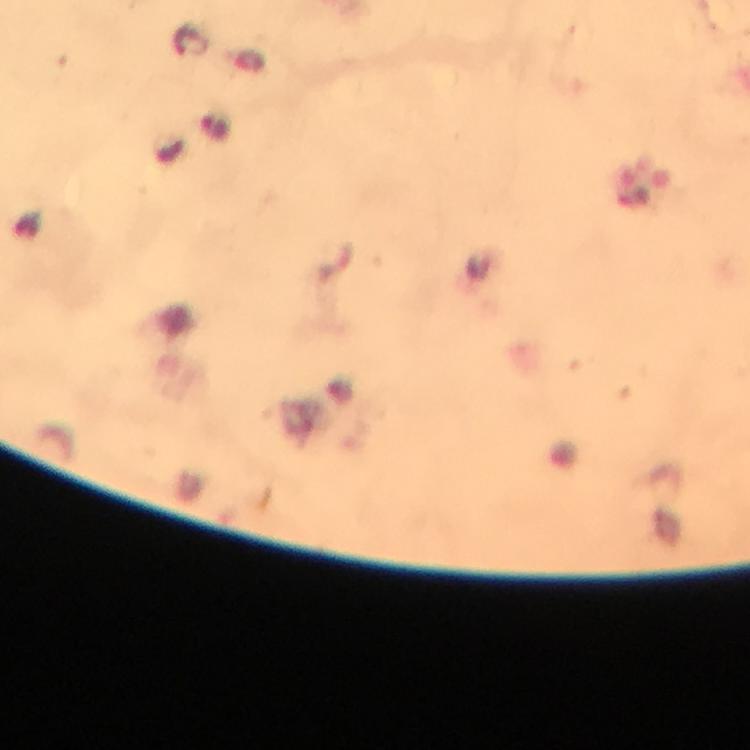
Approximate centers as (x, y) in pixels.
Summary:
  - Malaria parasite locations: (191, 45), (218, 127)
  - Immersion oil: applied
  - Cropped from: a single field of view
  - Preparation: thick blood film
  - Context: from a malaria diagnostic workup
  - Magnification: 100x
  - Image size: 750×750 pixels
  - Capture: smartphone camera through the microscope
  - Stain: Giemsa